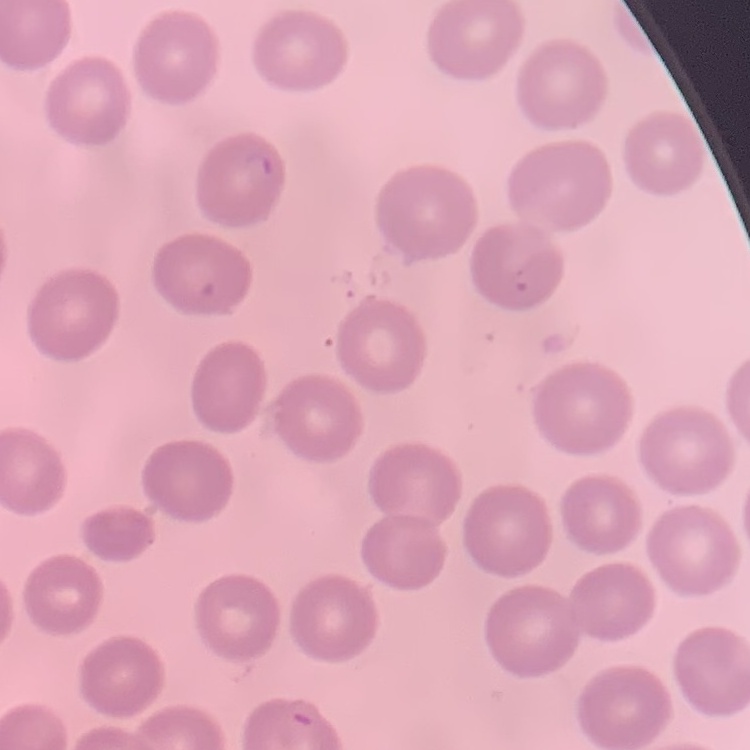

The erythrocytes exhibit no rouleaux formation. Square crop of a larger photomicrograph. Field's or Giemsa stain. Thin blood smear.